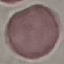

Result: negative for malaria parasites. Photographed with a smartphone camera at the microscope eyepiece. Automatically extracted cell patch, resized to 64 × 64 pixels. Giemsa stain. Thin smear of blood.